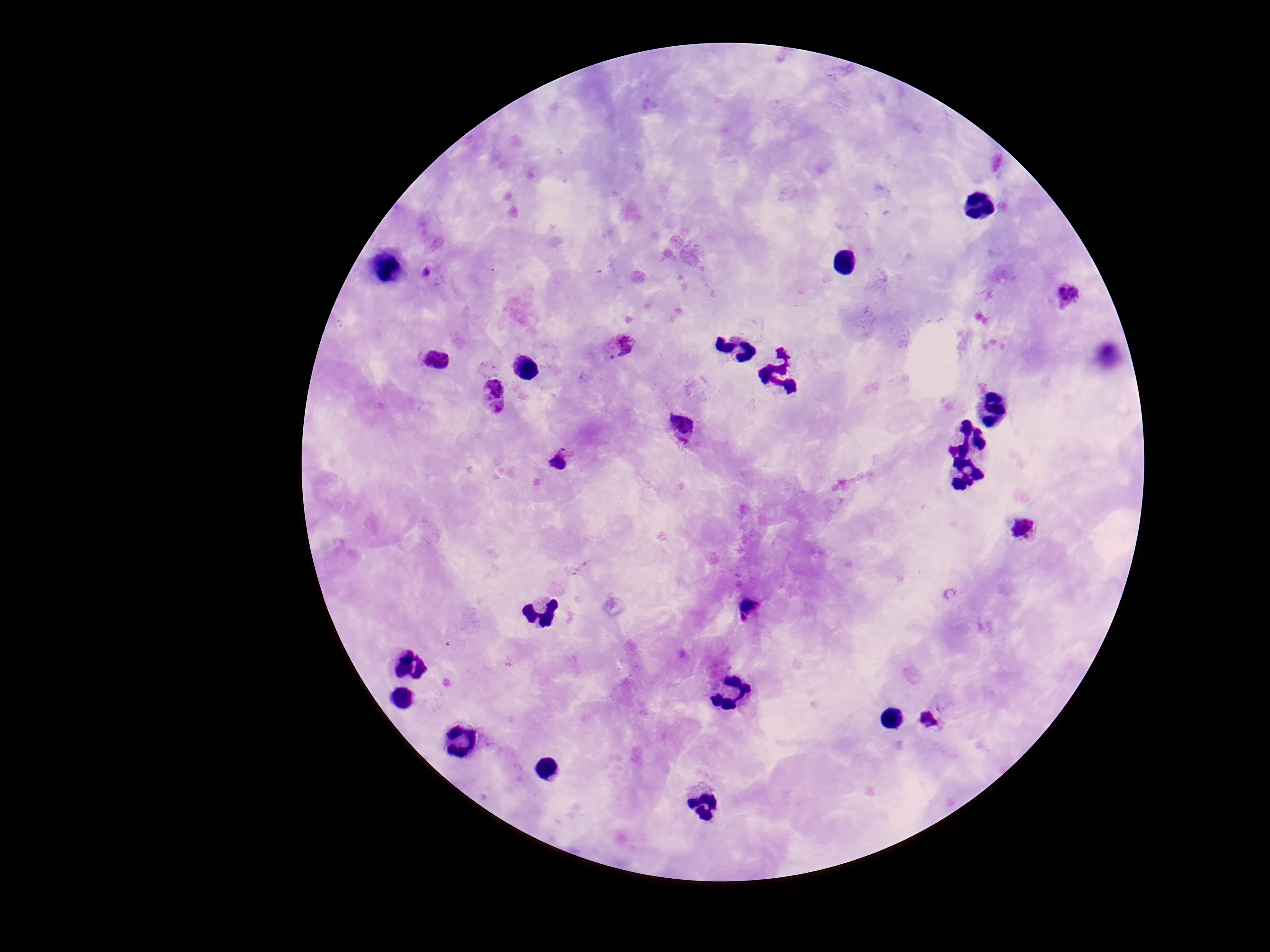
Approximate centers as (x, y) in pixels.
Summary:
  - Plasmodium parasite locations: (425, 273), (1068, 292), (617, 347), (437, 360), (496, 392), (684, 428), (560, 462), (1023, 528), (748, 608), (928, 721)
  - Preparation: thick blood film
  - Capture: smartphone camera through the microscope eyepiece
  - Field of view: one from this slide
  - Stain: Giemsa
  - Patient malaria status: infected
  - Magnification: 100x
  - Image size: 1270×952 pixels